State which parasite is depicted.
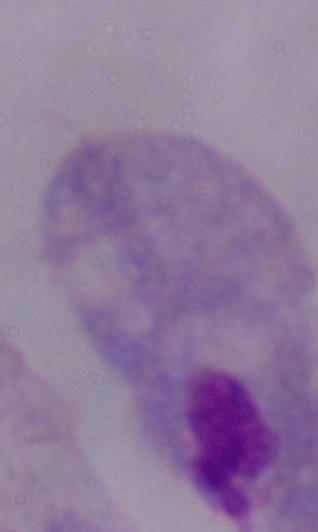
A trichomonad.

Photomicrograph. 1000x magnification.